Give the position of every Plasmodium parasite and every leukocyte.
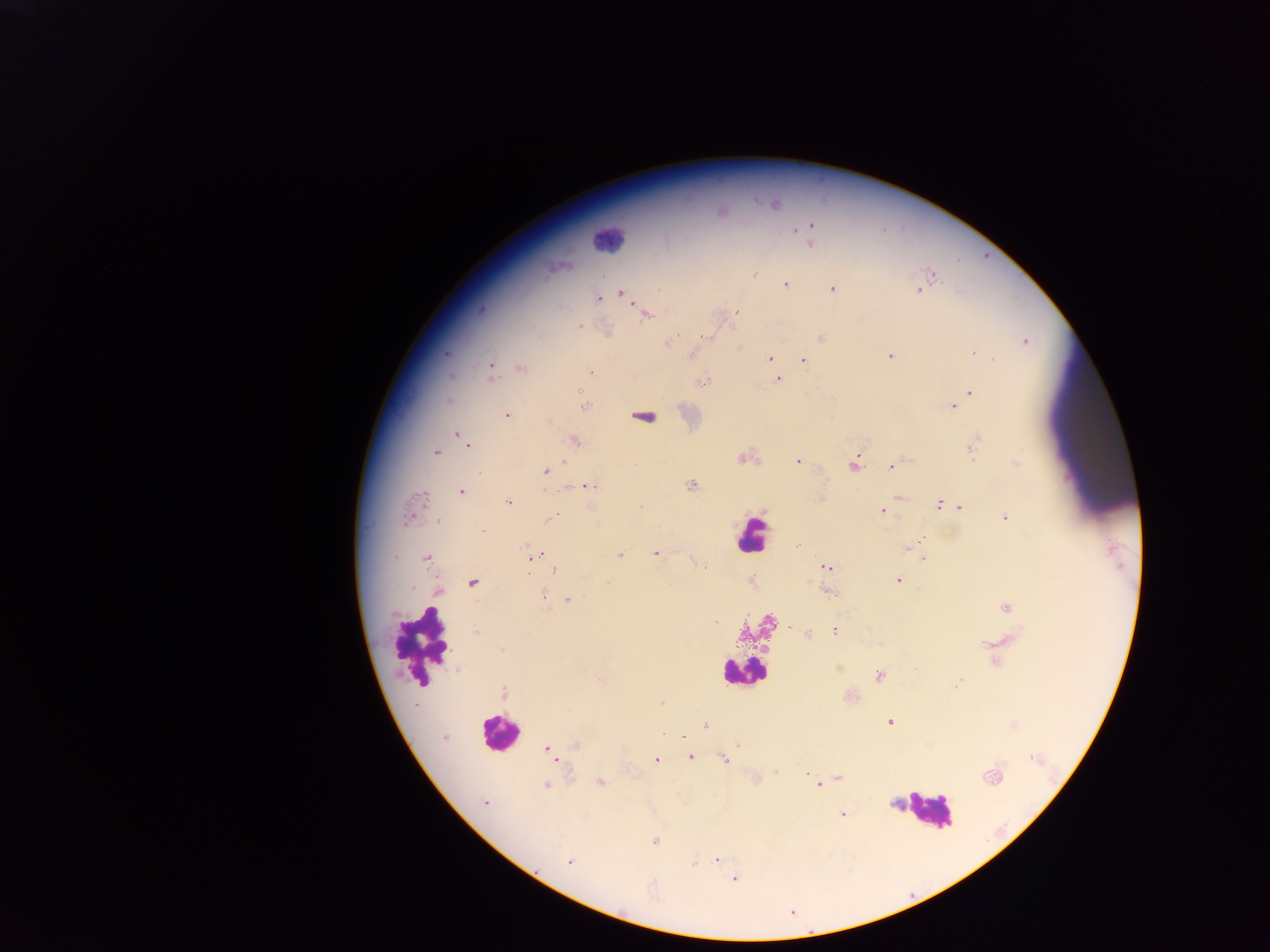
Approximate centers as x y in pixels.
Plasmodium parasites: 774 203; 719 210; 809 230; 810 242; 561 265; 754 274; 930 274; 603 276; 785 284; 833 287; 919 289; 621 293; 598 297; 629 298; 736 312; 646 314; 579 327; 731 328; 607 333; 709 336; 821 337; 1025 341; 667 343; 739 346; 446 352; 972 352; 693 354; 890 355; 770 358; 802 360; 993 360; 520 367; 774 368; 490 371; 590 371; 450 375; 778 379; 702 381; 577 391; 970 391; 448 401; 953 406; 582 407; 506 414; 642 417; 457 433; 575 441; 467 444; 974 444; 436 453; 743 457; 797 461; 853 462; 1016 463; 892 465; 544 471; 691 484; 587 485; 461 491; 899 497; 821 498; 509 502; 939 504; 640 506; 959 507; 883 511; 411 512; 1005 517; 549 518; 438 519; 796 545; 913 545; 907 548; 655 553; 619 555; 533 556; 426 557; 924 558; 703 566; 824 567; 555 568; 897 580; 751 581; 607 582; 472 583; 437 591; 828 592; 543 595; 567 600; 1006 606; 716 621; 835 630; 476 631; 807 634; 995 660; 880 675; 503 692; 889 721; 1012 724; 706 725; 444 737; 682 737; 576 744; 738 744; 547 750; 552 755; 690 756; 656 759; 724 759; 806 771; 776 772; 838 777; 824 780; 599 782; 546 784; 818 784; 485 802; 842 813; 654 841; 717 860; 569 861; 693 863; 734 878.
Leukocytes: 607 239; 752 534; 421 645; 744 672; 500 732; 927 812.

preparation = thick blood film
capture = mobile-phone photograph through a microscope
image size = 1270×952 pixels
country = Ghana
field of view = single